Assess the morphology of the erythrocytes.
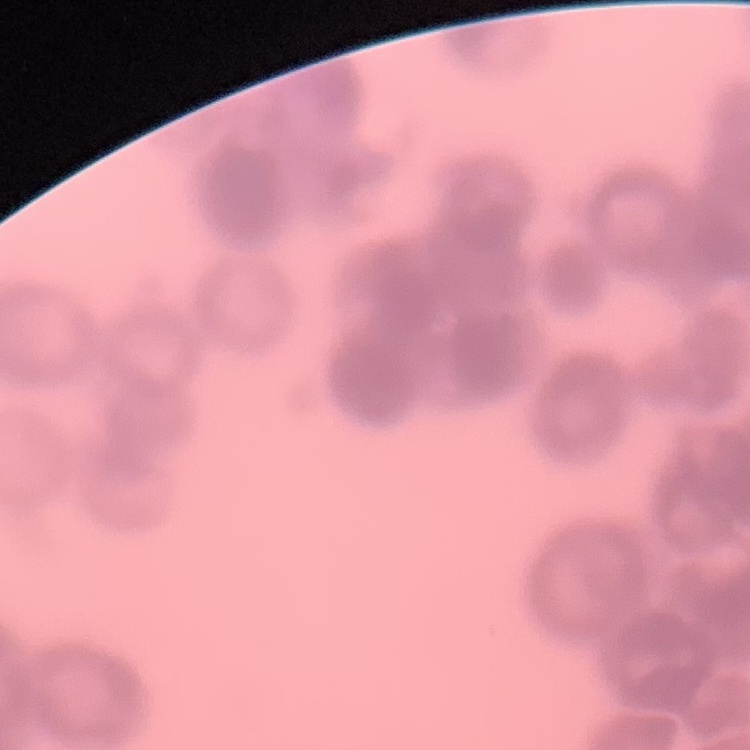
They show rouleaux formation.

stain = Field's or Giemsa
preparation = thin blood smear
image type = square crop of a larger photomicrograph